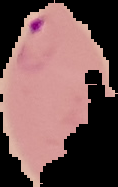

Summary:
  - Image size: 118×187 pixels
  - Preparation: thin blood smear
  - Malaria status: parasitized
  - Image type: segmented cell region with the area outside set to black